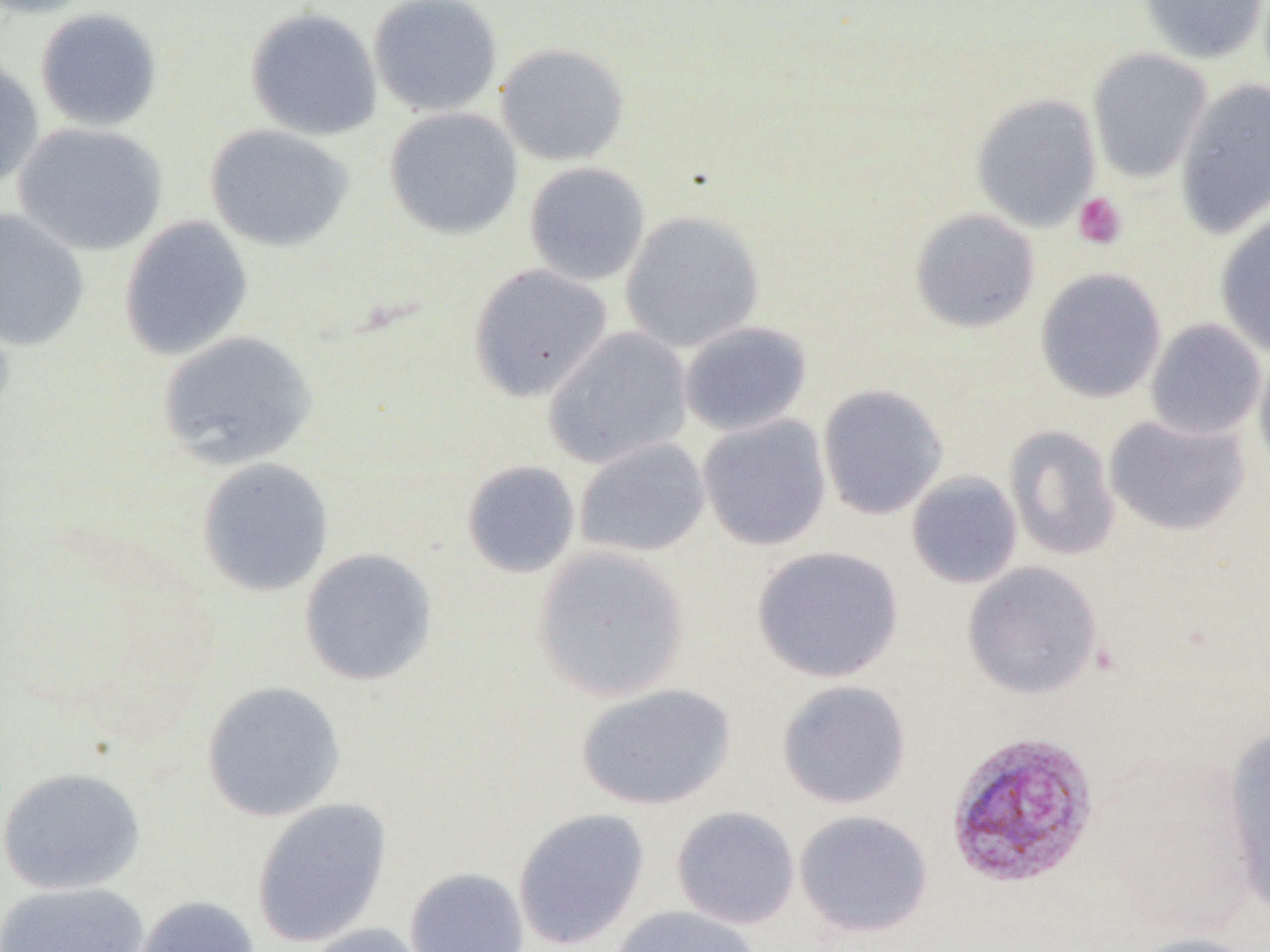

slide-level diagnosis = Plasmodium vivax
preparation = thin blood film
magnification = 1000x
field of view = single
image size = 1270×952 pixels
modality = light microscopy
Plasmodium vivax-infected red blood cell locations = approximate bounding boxes as (x1,y1)-(x2,y2) corner pairs in pixels: (944,730)-(1099,889)
uninfected red blood cell locations = approximate bounding boxes as (x1,y1)-(x2,y2) corner pairs in pixels: (0,0)-(100,19), (368,0)-(503,118), (1139,0)-(1268,64), (244,7)-(383,141), (34,8)-(163,131), (494,43)-(630,166), (1087,48)-(1213,184), (0,55)-(45,190), (1174,79)-(1270,240), (970,93)-(1102,232), (384,107)-(523,240), (13,122)-(168,256), (204,124)-(354,252), (524,162)-(651,286), (0,208)-(90,352), (909,208)-(1040,333), (619,210)-(765,352), (1214,213)-(1270,358), (118,216)-(254,361), (468,263)-(613,402), (1035,267)-(1167,404), (1145,318)-(1267,441), (679,321)-(812,436), (543,326)-(693,469), (157,330)-(317,470), (1253,349)-(1270,482), (817,383)-(949,520), (697,414)-(832,551), (1104,414)-(1250,536), (1004,425)-(1120,561), (573,438)-(711,558), (196,458)-(334,597), (461,460)-(581,578), (906,471)-(1023,589), (531,545)-(690,703), (751,546)-(904,683), (298,547)-(438,686), (963,561)-(1103,700), (777,680)-(912,809), (201,681)-(347,822), (574,683)-(737,810), (1222,722)-(1270,915), (0,765)-(145,895), (251,797)-(393,948), (670,806)-(801,929), (512,807)-(650,950), (793,810)-(934,938), (403,867)-(529,952), (0,882)-(150,952), (128,895)-(262,952), (608,905)-(761,952), (300,922)-(434,952), (1126,932)-(1262,952)
platelet locations = approximate bounding boxes as (x1,y1)-(x2,y2) corner pairs in pixels: (1072,192)-(1128,250)